Evaluate for Plasmodium parasites.
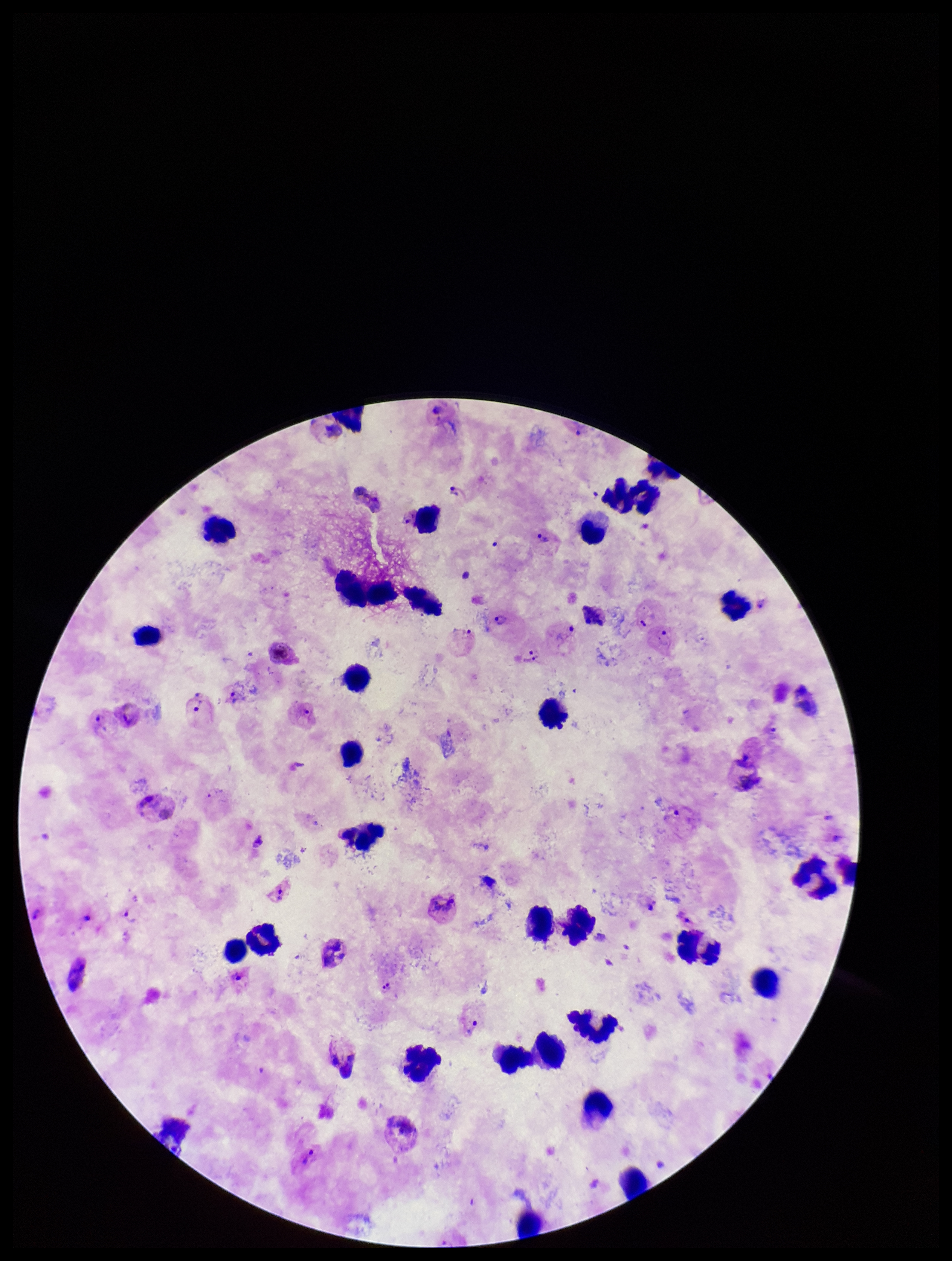
Detected.

Patient malaria status: positive. Preparation: thick smear. Image is 952×1261 pixels. Smartphone photograph taken through the eyepiece of a microscope. Parasite count: 14. Leukocyte count: 27. One field from this slide. Giemsa stain. Species reported for this patient: Plasmodium vivax.